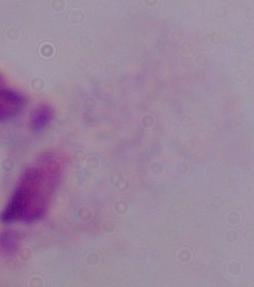

{
  "modality": "photomicrograph",
  "identification": "trichomonad",
  "magnification": "1000x"
}